State the preparation type.
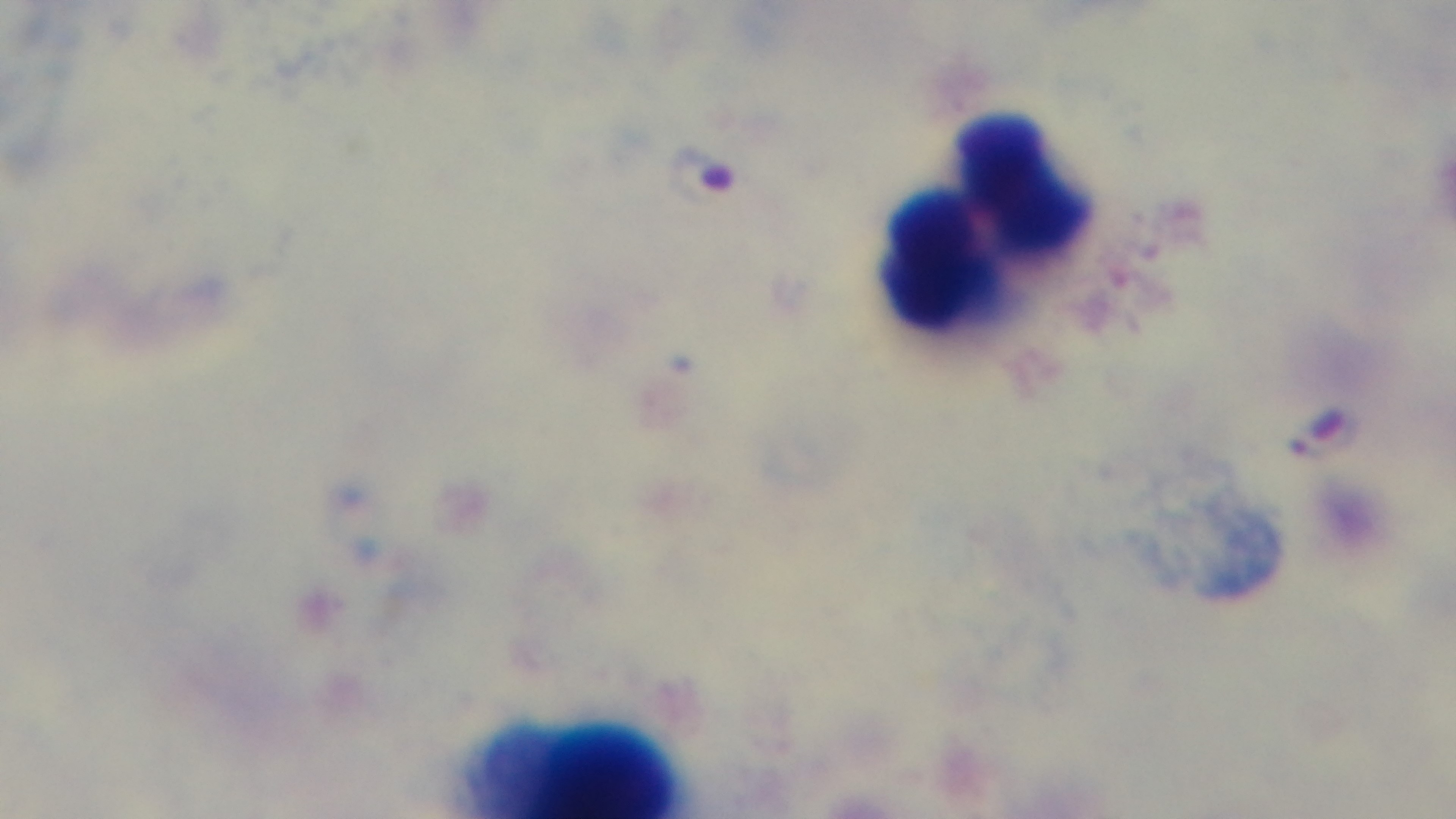

Thick.

Malaria status: positive. Giemsa-stained. Mounted 4K digital camera. Light microscopy. Oil-immersion objective, 100x. One field from the slide.